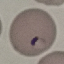

result = malaria parasites detected
stain = Giemsa
image type = cell patch, automatically extracted from a larger field of view and resized to 64 × 64 pixels
preparation = thin smear
capture = smartphone camera at the microscope eyepiece